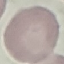
Malaria status: uninfected. Cell patch, automatically extracted from a larger field of view and resized to 64 × 64 pixels. Acquired by smartphone through the microscope eyepiece. Giemsa stain. Thin blood smear.